Identify the blood parasite species.
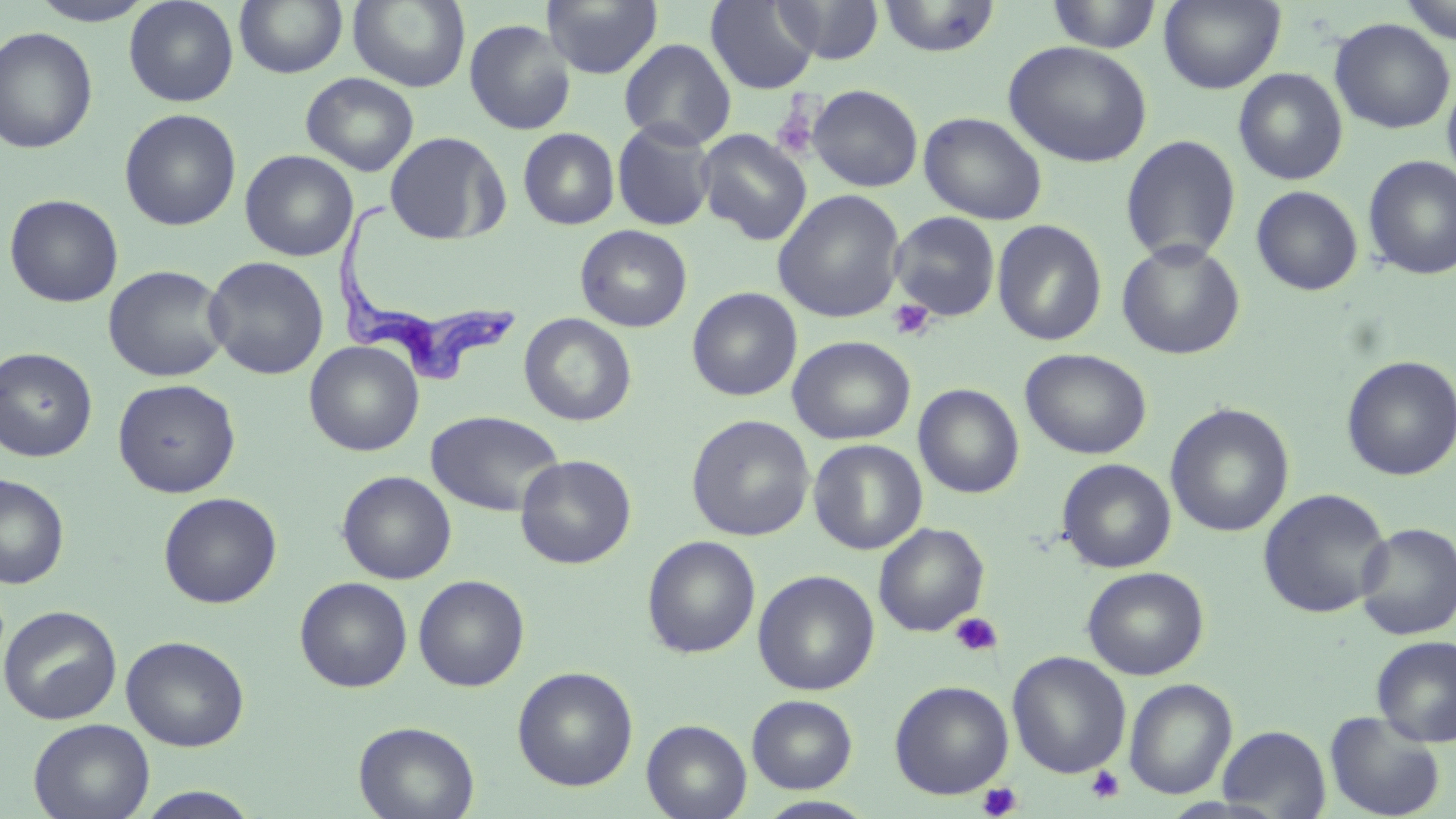

Trypanosoma brucei.

Summary:
  - Coordinate format: approximate bounding boxes as [x1, y1, x2, y2] in pixels
  - Uninfected red blood cell locations: [25, 0, 160, 26], [234, 0, 348, 78], [347, 0, 471, 91], [774, 0, 885, 64], [878, 0, 1000, 58], [1159, 0, 1286, 94], [1397, 0, 1456, 44], [124, 1, 239, 107], [541, 1, 663, 80], [706, 1, 820, 94], [1046, 1, 1163, 53], [464, 18, 576, 135], [1329, 18, 1455, 134], [0, 26, 98, 154], [619, 38, 736, 150], [1003, 41, 1153, 168], [1233, 67, 1348, 185], [301, 72, 419, 176], [1442, 72, 1456, 187], [807, 84, 923, 192], [119, 108, 241, 231], [919, 111, 1047, 225], [612, 118, 716, 231], [518, 128, 620, 230], [696, 129, 812, 245], [384, 131, 510, 246], [1120, 134, 1242, 265], [239, 149, 358, 262], [1362, 155, 1456, 280], [1251, 185, 1364, 296], [772, 189, 906, 323], [3, 194, 124, 308], [888, 211, 1001, 322], [992, 220, 1107, 346], [575, 224, 693, 332], [1116, 239, 1246, 360], [203, 256, 329, 379], [102, 264, 231, 382], [686, 287, 802, 401], [519, 313, 637, 426], [787, 336, 916, 445], [304, 341, 423, 456], [0, 347, 97, 462], [1020, 348, 1152, 459], [1340, 355, 1456, 481], [113, 379, 240, 498], [913, 383, 1025, 499], [1165, 403, 1295, 538], [426, 410, 565, 517], [686, 414, 815, 541], [808, 439, 927, 555], [515, 454, 637, 569], [1056, 458, 1176, 573], [337, 470, 456, 584], [0, 474, 70, 589], [1257, 488, 1393, 619], [158, 491, 282, 608], [873, 522, 989, 637], [1355, 522, 1456, 640], [642, 535, 761, 658], [1082, 566, 1209, 680], [753, 570, 880, 695], [413, 574, 530, 691], [295, 577, 412, 692], [0, 605, 122, 725], [121, 635, 249, 752], [1371, 635, 1456, 747], [1007, 651, 1131, 778], [512, 666, 638, 791], [1124, 678, 1237, 800], [889, 680, 1014, 799], [747, 694, 858, 793], [640, 710, 857, 807], [1324, 711, 1446, 819], [28, 718, 155, 819], [641, 719, 752, 819], [353, 721, 480, 819], [1217, 724, 1332, 818], [132, 787, 263, 819], [754, 796, 878, 818]
  - Trypanosoma brucei locations: [334, 193, 518, 390]
  - Platelet locations: [771, 101, 820, 160], [888, 298, 935, 342], [949, 612, 1003, 657], [1086, 766, 1125, 804], [978, 782, 1022, 819]
  - Image size: 1456×819 pixels
  - Stain: May-Grünwald-Giemsa
  - Field of view: one of a larger specimen
  - Preparation: thin blood film
  - Magnification: 1000x
  - Modality: optical microscopy